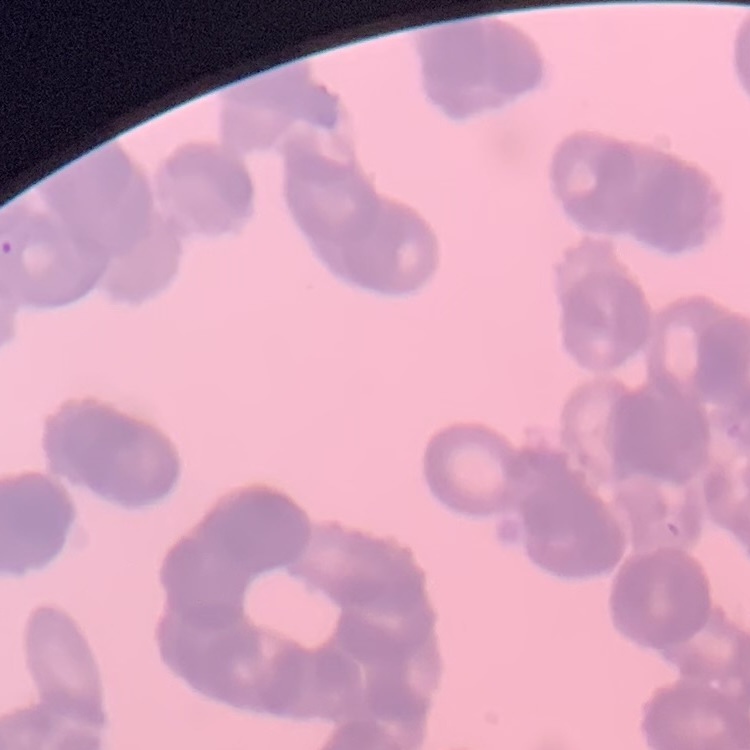 The red blood cells exhibit rouleaux formation. Thin peripheral smear. Stained with either Field's or Giemsa. Square crop of a larger photomicrograph.